Locate and identify every blood parasite.
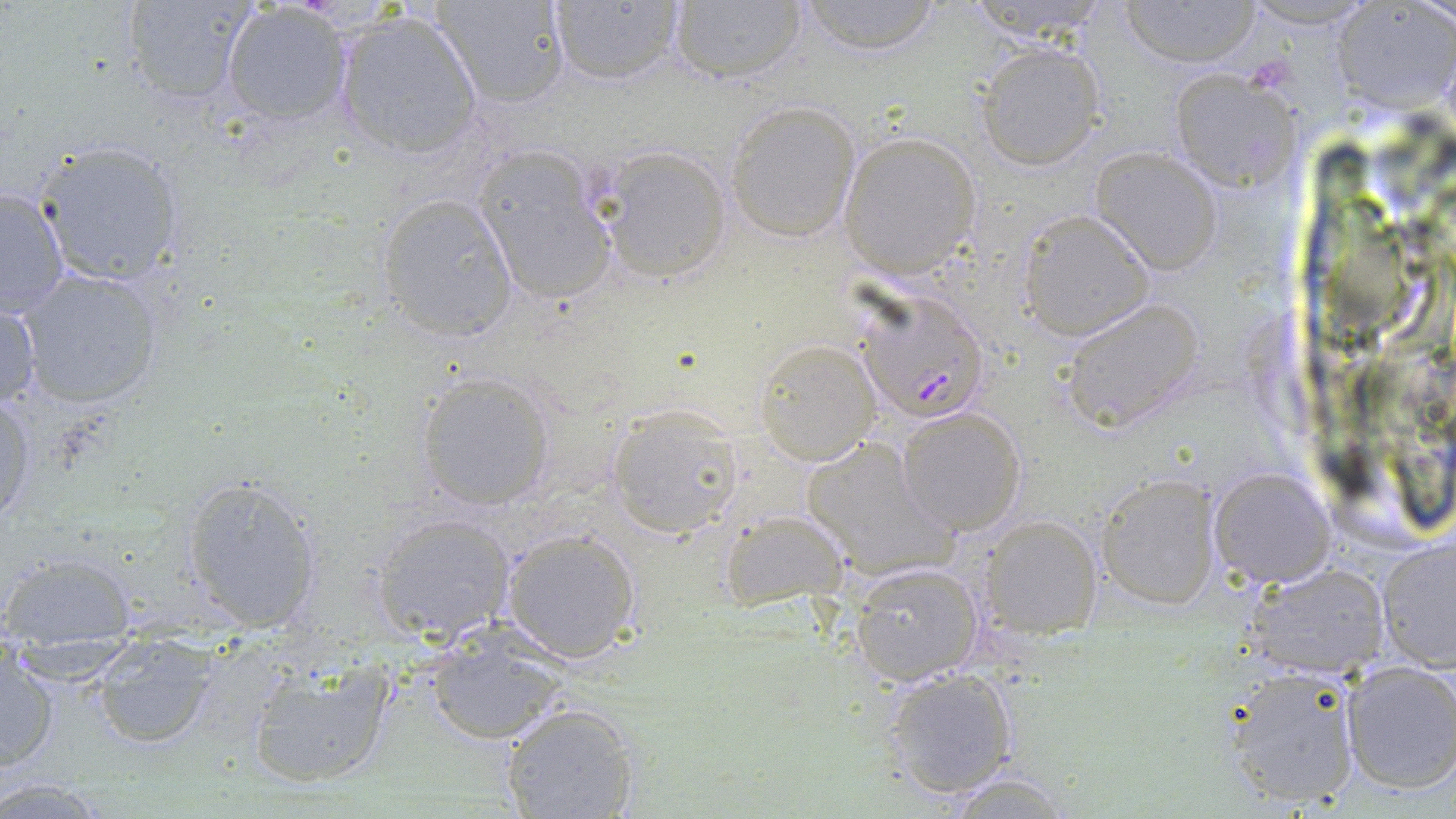
Approximate bounding boxes as named x1/y1/x2/y2 corners in pixels.
Plasmodium falciparum-infected red blood cells: (x1=854, y1=293, x2=989, y2=424).
No Plasmodium ovale, Plasmodium malariae, Plasmodium vivax, Babesia divergens, or Trypanosoma brucei observed.

Summary:
  - Uninfected red blood cell locations: (x1=121, y1=0, x2=259, y2=107), (x1=431, y1=0, x2=571, y2=107), (x1=543, y1=0, x2=685, y2=89), (x1=666, y1=0, x2=810, y2=86), (x1=1120, y1=0, x2=1259, y2=67), (x1=1237, y1=0, x2=1383, y2=27), (x1=794, y1=1, x2=945, y2=54), (x1=219, y1=3, x2=354, y2=125), (x1=1335, y1=3, x2=1455, y2=111), (x1=332, y1=10, x2=484, y2=161), (x1=976, y1=42, x2=1105, y2=169), (x1=1166, y1=66, x2=1300, y2=192), (x1=724, y1=101, x2=861, y2=242), (x1=839, y1=131, x2=983, y2=279), (x1=34, y1=138, x2=188, y2=288), (x1=594, y1=144, x2=733, y2=283), (x1=470, y1=145, x2=621, y2=307), (x1=1089, y1=147, x2=1224, y2=275), (x1=0, y1=185, x2=70, y2=319), (x1=375, y1=192, x2=518, y2=341), (x1=1018, y1=210, x2=1152, y2=340), (x1=15, y1=268, x2=165, y2=411), (x1=0, y1=296, x2=42, y2=418), (x1=1059, y1=297, x2=1208, y2=434), (x1=756, y1=338, x2=880, y2=463), (x1=417, y1=371, x2=554, y2=511), (x1=0, y1=391, x2=36, y2=526), (x1=606, y1=404, x2=743, y2=536), (x1=895, y1=406, x2=1026, y2=535), (x1=803, y1=436, x2=957, y2=581), (x1=1208, y1=468, x2=1335, y2=587), (x1=1095, y1=473, x2=1222, y2=611), (x1=181, y1=475, x2=322, y2=635), (x1=722, y1=507, x2=850, y2=607), (x1=371, y1=513, x2=516, y2=643), (x1=978, y1=516, x2=1101, y2=638), (x1=500, y1=527, x2=641, y2=662), (x1=1376, y1=537, x2=1456, y2=669), (x1=2, y1=552, x2=135, y2=641), (x1=850, y1=562, x2=985, y2=685), (x1=1246, y1=563, x2=1391, y2=677), (x1=428, y1=632, x2=565, y2=744), (x1=91, y1=637, x2=224, y2=750), (x1=0, y1=652, x2=58, y2=770), (x1=243, y1=659, x2=394, y2=790), (x1=1339, y1=660, x2=1455, y2=794), (x1=1222, y1=665, x2=1364, y2=809), (x1=880, y1=667, x2=1017, y2=798), (x1=498, y1=703, x2=641, y2=819), (x1=937, y1=771, x2=1078, y2=818), (x1=0, y1=779, x2=117, y2=815)
  - Slide-level diagnosis: Plasmodium falciparum
  - Image size: 1456×819 pixels
  - Preparation: thin blood smear
  - Stain: May-Grünwald-Giemsa
  - Modality: light microscopy
  - Magnification: 1000x
  - Field of view: single